Identify the parasite.
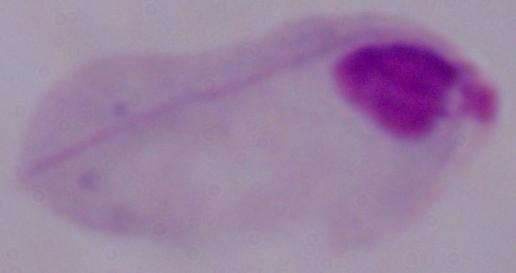

A trichomonad.

magnification = 1000x
modality = photomicrograph